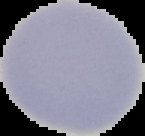 Image is 145×136 pixels. Malaria status: uninfected. From a thin blood film. Cell region segmented out of the field of view; the surrounding area is masked to black.